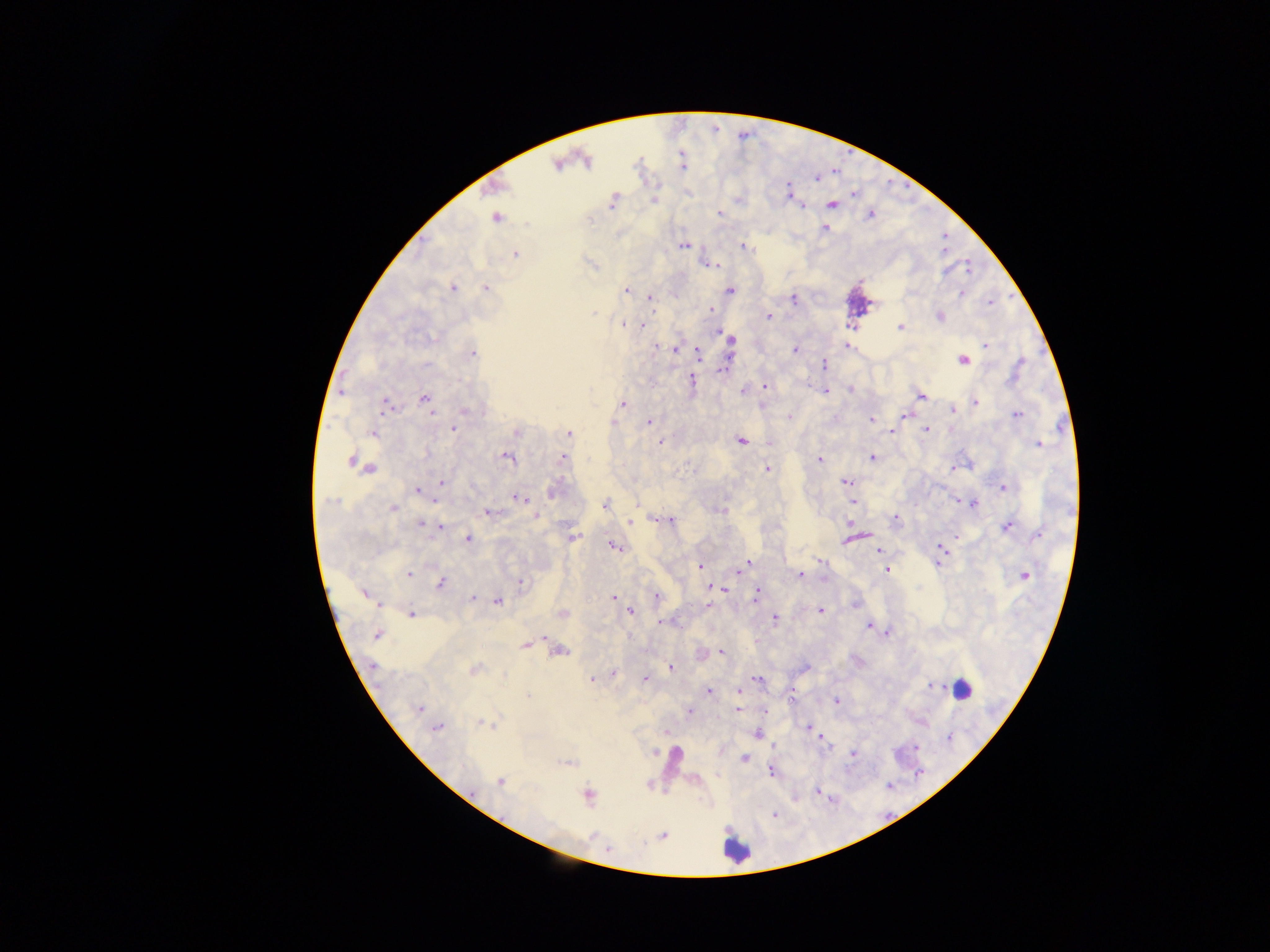
country = Ghana
capture = mobile-phone photograph through a microscope
field of view = single
leukocyte locations = approximate centers as x y in pixels: 962 688; 737 849
image size = 1270×952 pixels
preparation = thick blood smear
malaria parasite locations = approximate centers as x y in pixels: 583 159; 557 164; 788 192; 854 194; 612 201; 654 201; 804 205; 831 205; 719 213; 869 214; 495 217; 824 228; 684 246; 742 247; 514 253; 713 265; 452 287; 486 289; 626 290; 729 290; 962 291; 649 297; 793 299; 990 302; 653 310; 709 310; 768 316; 940 316; 622 323; 630 324; 641 325; 900 328; 720 333; 729 340; 986 344; 846 345; 675 349; 795 350; 471 352; 698 353; 962 360; 823 365; 725 367; 692 381; 764 386; 851 390; 744 391; 825 391; 921 395; 424 398; 974 402; 622 403; 385 405; 952 409; 465 410; 1016 415; 788 416; 871 420; 648 422; 453 428; 925 429; 890 431; 373 433; 568 433; 740 440; 661 442; 1038 443; 506 457; 870 457; 562 458; 819 460; 352 461; 366 467; 766 469; 953 469; 845 481; 441 482; 1002 486; 417 490; 553 491; 519 497; 957 500; 435 501; 852 502; 638 503; 604 504; 972 504; 393 508; 722 510; 489 512; 535 516; 894 518; 660 519; 671 520; 636 521; 629 522; 420 523; 441 526; 1007 526; 956 534; 1038 534; 572 537; 847 538; 468 539; 615 547; 941 548; 878 550; 820 561; 747 563; 939 564; 699 567; 739 567; 886 569; 409 574; 800 574; 1025 574; 519 582; 440 583; 724 590; 365 593; 756 594; 613 597; 657 597; 471 598; 497 600; 855 604; 378 605; 708 606; 820 610; 631 611; 412 613; 562 613; 774 618; 661 622; 869 625; 887 631; 377 635; 543 637; 526 644; 557 651; 721 651; 669 667; 474 668; 613 672; 592 677; 645 679; 757 680; 932 686; 709 692; 739 692; 528 695; 835 702; 418 709; 737 709; 688 711; 485 723; 807 727; 436 728; 758 733; 820 736; 916 749; 853 753; 743 758; 771 771; 500 781; 818 790; 588 795; 775 814; 663 835